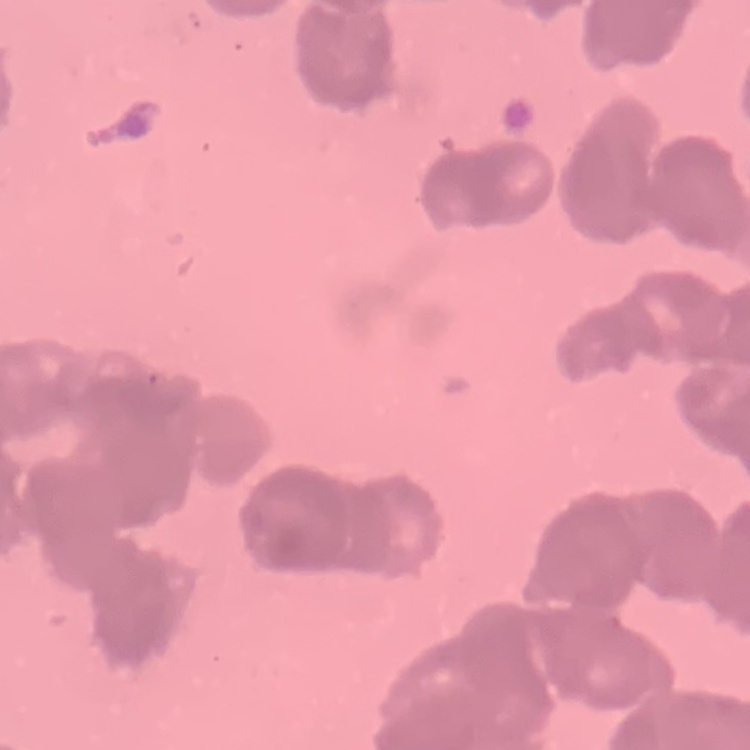

The erythrocytes exhibit rouleaux formation. Thin peripheral smear. One tile cut from a larger photomicrograph. Field's or Giemsa stain.